Locate and identify every blood parasite.
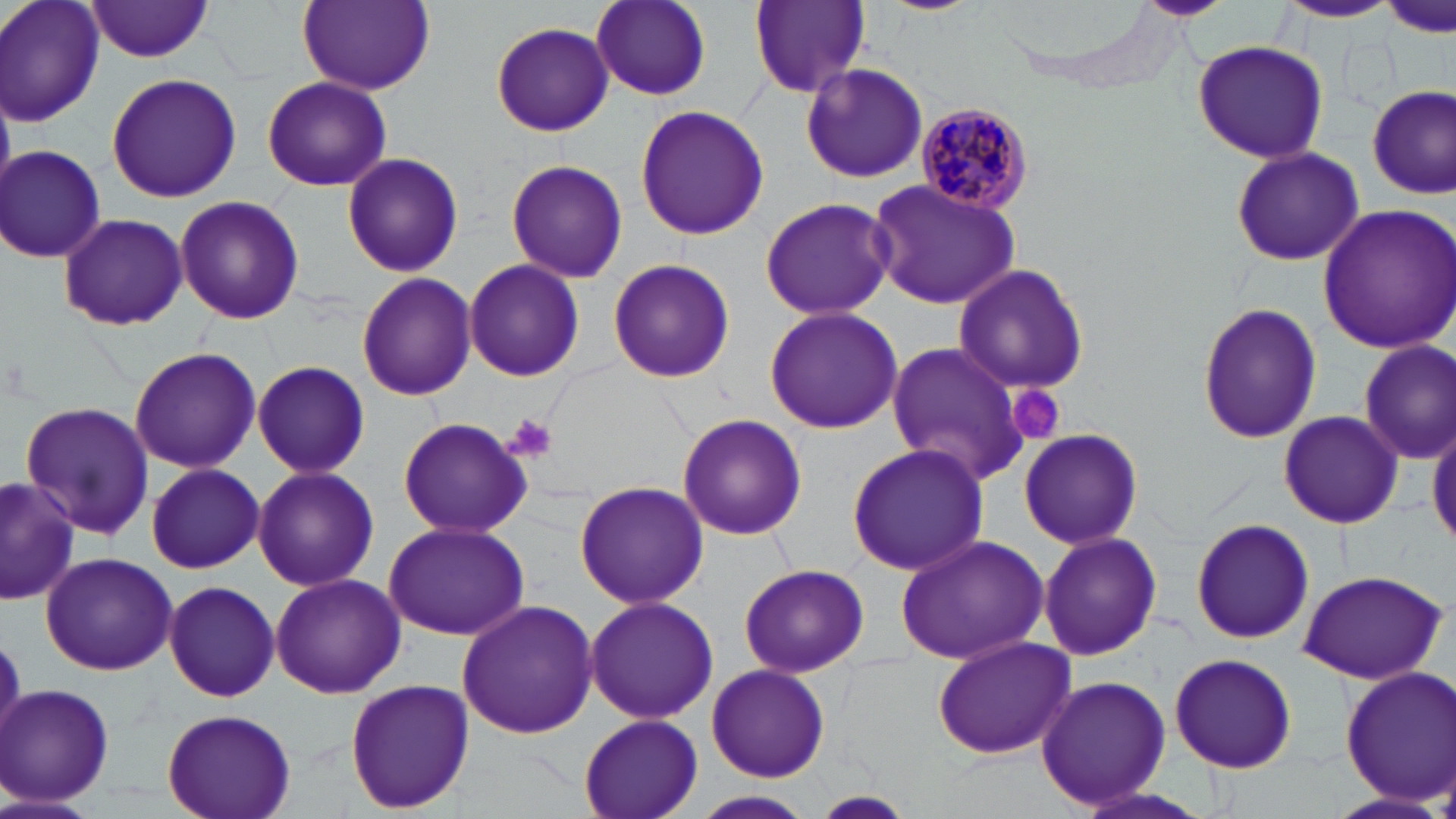

Approximate bounding boxes as named x1/y1/x2/y2 corners in pixels.
Plasmodium malariae-infected red blood cells: (x1=911, y1=102, x2=1034, y2=219).
No Plasmodium falciparum, Plasmodium ovale, Plasmodium vivax, Babesia divergens, or Trypanosoma brucei observed.

Uninfected red blood cell locations: (x1=1, y1=0, x2=105, y2=128), (x1=749, y1=0, x2=868, y2=95), (x1=880, y1=0, x2=980, y2=15), (x1=1130, y1=0, x2=1236, y2=21), (x1=298, y1=1, x2=436, y2=96), (x1=592, y1=1, x2=712, y2=101), (x1=85, y1=2, x2=216, y2=62), (x1=1274, y1=2, x2=1399, y2=24), (x1=489, y1=22, x2=615, y2=137), (x1=1192, y1=40, x2=1330, y2=164), (x1=800, y1=64, x2=927, y2=184), (x1=106, y1=73, x2=243, y2=202), (x1=261, y1=74, x2=392, y2=192), (x1=1368, y1=85, x2=1454, y2=200), (x1=633, y1=104, x2=769, y2=240), (x1=1, y1=145, x2=106, y2=263), (x1=1230, y1=145, x2=1364, y2=267), (x1=341, y1=152, x2=464, y2=278), (x1=506, y1=159, x2=628, y2=283), (x1=866, y1=177, x2=1024, y2=310), (x1=175, y1=195, x2=304, y2=324), (x1=759, y1=197, x2=895, y2=319), (x1=1315, y1=201, x2=1456, y2=355), (x1=56, y1=212, x2=189, y2=331), (x1=608, y1=259, x2=735, y2=384), (x1=464, y1=260, x2=585, y2=382), (x1=954, y1=265, x2=1091, y2=395), (x1=357, y1=273, x2=477, y2=400), (x1=1196, y1=302, x2=1321, y2=445), (x1=762, y1=306, x2=905, y2=434), (x1=883, y1=338, x2=1029, y2=486), (x1=1357, y1=339, x2=1456, y2=464), (x1=128, y1=348, x2=261, y2=472), (x1=252, y1=361, x2=371, y2=478), (x1=20, y1=402, x2=155, y2=543), (x1=1278, y1=411, x2=1403, y2=530), (x1=676, y1=412, x2=808, y2=541), (x1=1429, y1=413, x2=1456, y2=549), (x1=398, y1=416, x2=531, y2=538), (x1=1016, y1=428, x2=1142, y2=548), (x1=846, y1=443, x2=991, y2=577), (x1=145, y1=462, x2=263, y2=573), (x1=252, y1=464, x2=379, y2=592), (x1=2, y1=479, x2=87, y2=604), (x1=574, y1=479, x2=709, y2=611), (x1=1189, y1=516, x2=1315, y2=647), (x1=381, y1=521, x2=527, y2=640), (x1=1038, y1=531, x2=1162, y2=661), (x1=896, y1=534, x2=1048, y2=665), (x1=40, y1=553, x2=178, y2=676), (x1=739, y1=562, x2=869, y2=678), (x1=1296, y1=569, x2=1449, y2=685), (x1=269, y1=573, x2=406, y2=699), (x1=162, y1=579, x2=282, y2=703), (x1=583, y1=596, x2=720, y2=725), (x1=456, y1=600, x2=597, y2=740), (x1=930, y1=634, x2=1076, y2=760), (x1=1170, y1=650, x2=1297, y2=773), (x1=706, y1=664, x2=830, y2=783), (x1=1339, y1=665, x2=1454, y2=802), (x1=1034, y1=675, x2=1172, y2=812), (x1=344, y1=678, x2=475, y2=814), (x1=3, y1=683, x2=116, y2=808), (x1=161, y1=706, x2=296, y2=819), (x1=578, y1=712, x2=704, y2=819), (x1=1327, y1=790, x2=1451, y2=819), (x1=696, y1=791, x2=814, y2=818), (x1=814, y1=792, x2=916, y2=816). Platelet locations: (x1=1006, y1=387, x2=1065, y2=447), (x1=505, y1=411, x2=559, y2=463). Slide-level diagnosis: Plasmodium malariae. Thin blood smear. Single field of view. Captured at 1000x magnification. Image is 1456×819 pixels. Optical microscopy. May-Grünwald-Giemsa-stained preparation.